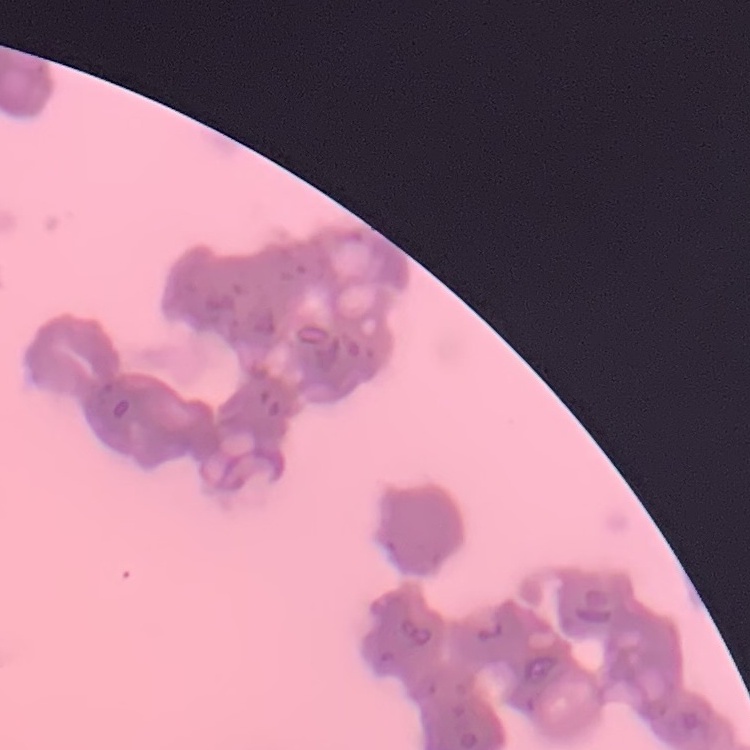

The red blood cells exhibit rouleaux formation. Thin peripheral smear. Square crop of a larger photomicrograph. Field's or Giemsa stain.